Locate every Plasmodium parasite.
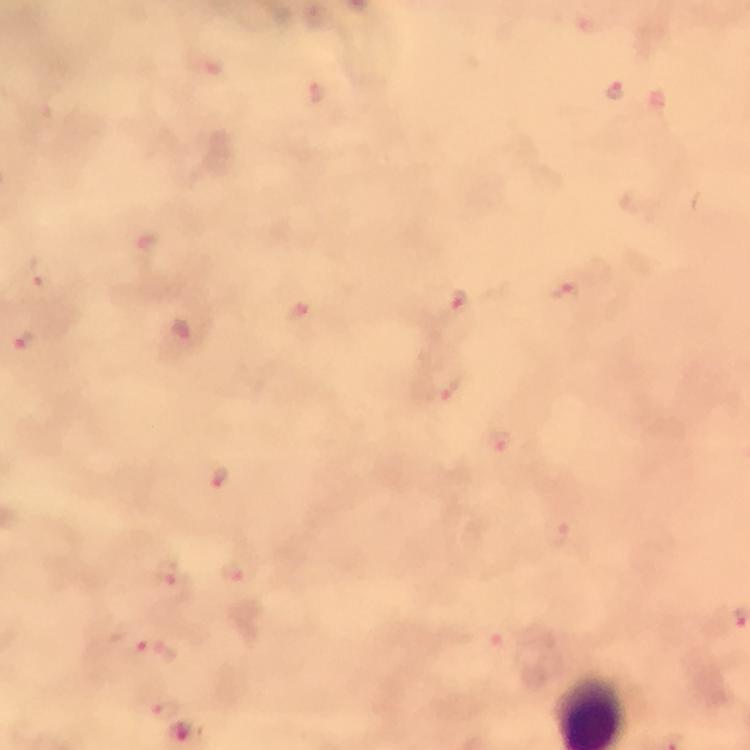

Approximate object centers, in pixels from the top-left corner.
Plasmodium parasites: (x=615, y=89), (x=317, y=93), (x=147, y=249), (x=563, y=291), (x=457, y=302), (x=181, y=330), (x=22, y=342), (x=452, y=389), (x=499, y=442), (x=220, y=479), (x=558, y=532), (x=235, y=572), (x=172, y=579), (x=495, y=641), (x=152, y=651), (x=166, y=711).

{
  "cropped_from": "a single field of view",
  "magnification": "100x",
  "capture": "smartphone camera through the microscope",
  "preparation": "thick smear",
  "stain": "Giemsa",
  "immersion_oil": "applied",
  "image_size": "750×750 pixels",
  "context": "from a diagnostic examination for malaria"
}